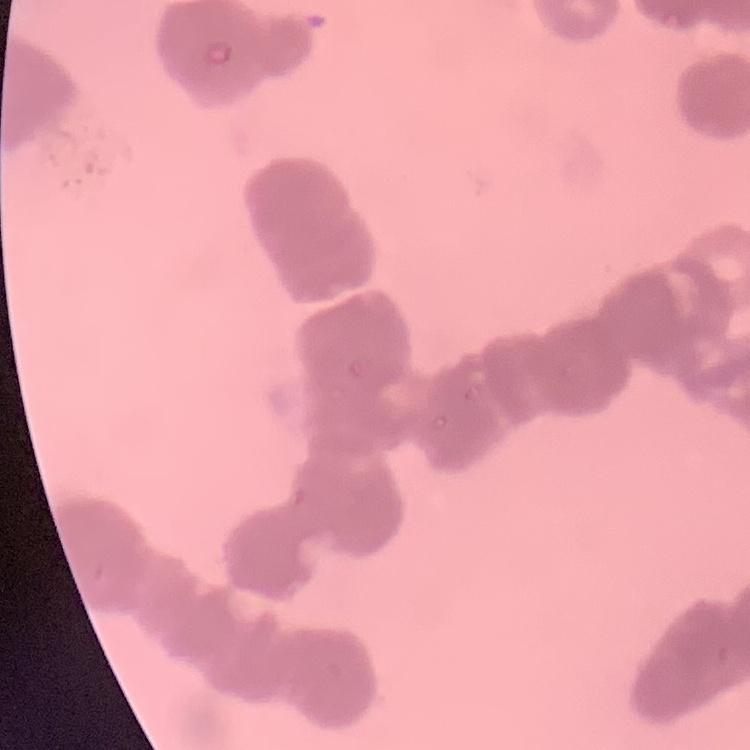
Summary:
  - Red blood cell morphology: rouleaux formation
  - Image type: one tile cut from a larger photomicrograph
  - Stain: Field's or Giemsa
  - Preparation: thin blood smear